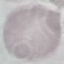

Result: negative for malaria parasites. Giemsa stain. Thin blood film. Automatically extracted cell patch, resized to 64 × 64 pixels. Photographed with a smartphone camera at the microscope eyepiece.